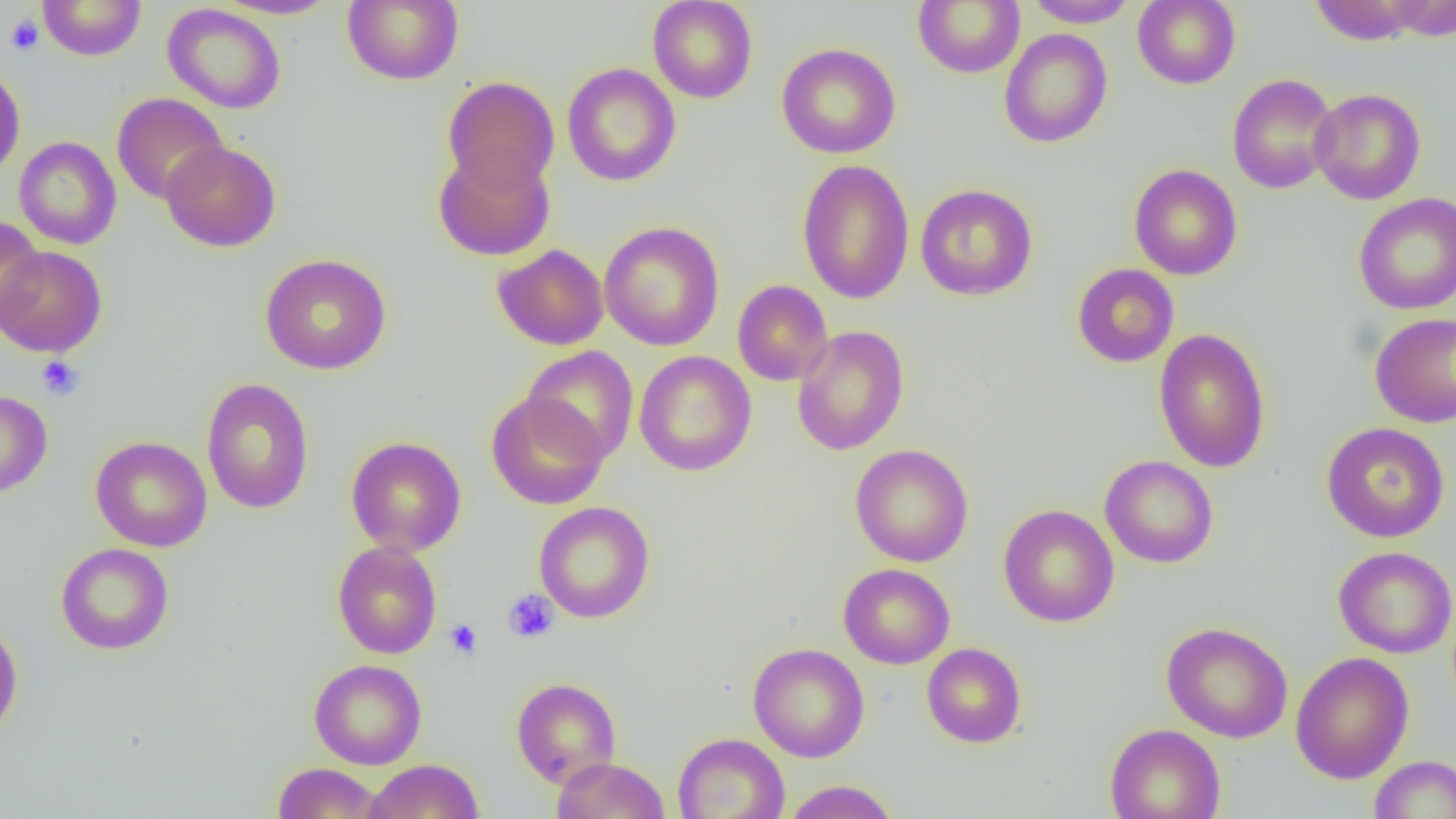
Approximate bounding boxes as (x1,y1)-(x2,y2) corner pairs in pixels. Platelet locations: (5,14)-(44,56), (37,356)-(85,400), (502,589)-(559,644), (444,619)-(482,659). Uninfected red blood cell locations: (38,0)-(146,60), (215,0)-(340,20), (342,0)-(463,86), (647,0)-(758,103), (1022,0)-(1140,28), (1132,0)-(1240,89), (1380,0)-(1456,41), (913,1)-(1025,78), (1308,1)-(1422,45), (162,3)-(287,114), (998,28)-(1112,148), (776,42)-(901,158), (0,63)-(25,182), (561,63)-(681,186), (1226,73)-(1340,194), (443,76)-(560,193), (1309,88)-(1426,205), (112,92)-(228,205), (14,136)-(122,250), (161,141)-(282,252), (433,148)-(555,261), (797,159)-(915,304), (1129,164)-(1243,280), (915,184)-(1038,301), (1353,193)-(1456,315), (0,216)-(44,330), (599,221)-(725,351), (0,244)-(107,357), (493,244)-(609,350), (260,254)-(392,375), (1072,263)-(1179,367), (732,280)-(833,386), (1370,312)-(1456,428), (791,325)-(910,456), (1153,328)-(1271,473), (522,346)-(639,463), (634,351)-(756,476), (201,378)-(315,514), (0,390)-(53,497), (486,391)-(609,510), (1321,422)-(1450,543), (90,435)-(212,552), (346,436)-(466,557), (850,444)-(974,567), (1100,455)-(1218,568), (534,501)-(655,623), (998,504)-(1119,627), (332,541)-(442,659), (55,542)-(174,655), (1333,546)-(1456,658), (838,563)-(955,669), (0,618)-(23,739), (1162,621)-(1293,743), (748,643)-(869,762), (921,643)-(1026,747), (1289,651)-(1414,784), (308,658)-(427,770), (511,677)-(621,787), (1104,723)-(1226,819), (672,732)-(790,819), (1369,755)-(1456,818), (552,757)-(670,819), (364,759)-(485,819), (272,762)-(385,818), (781,780)-(900,818). Slide-level diagnosis: negative for blood parasites. Single field of view. Optical microscopy. Thin blood smear. Image is 1456×819 pixels. 1000x magnification.